Outline each blood parasite and name the species.
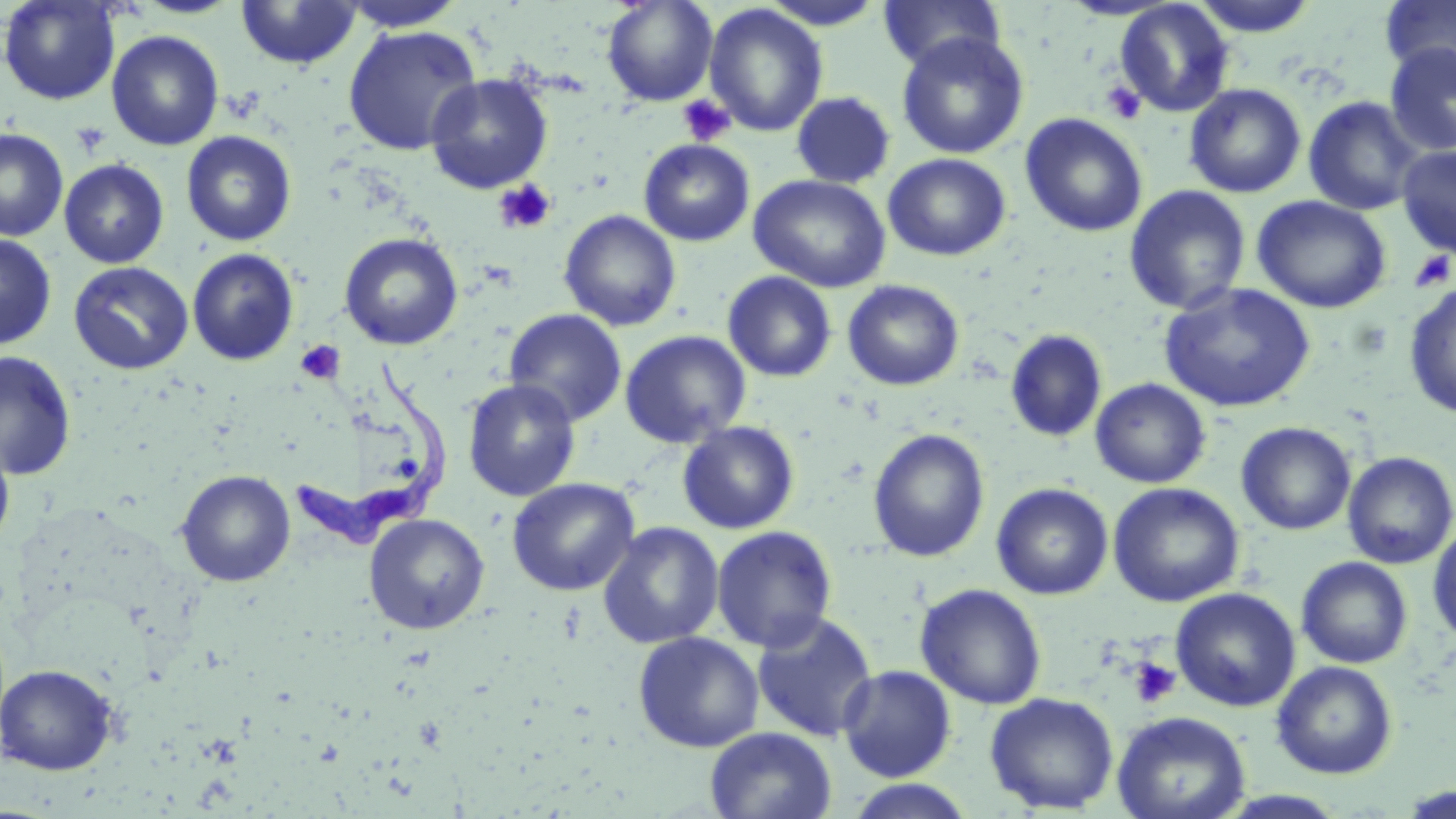

Approximate bounding boxes as (x1,y1)-(x2,y2) corner pairs in pixels.
Trypanosoma brucei: (289,361)-(452,548).
No Plasmodium falciparum, Plasmodium ovale, Plasmodium malariae, Plasmodium vivax, or Babesia divergens observed.

Summary:
  - Uninfected red blood cell locations: (0,0)-(121,105), (133,0)-(243,19), (339,0)-(464,32), (601,0)-(718,106), (758,0)-(886,29), (879,0)-(1005,72), (1059,0)-(1180,21), (1189,0)-(1320,37), (1379,0)-(1456,84), (235,1)-(362,70), (1114,1)-(1235,117), (703,4)-(829,137), (342,24)-(482,155), (106,30)-(224,151), (896,32)-(1029,160), (1384,42)-(1456,156), (425,73)-(553,194), (1184,83)-(1306,198), (791,92)-(895,188), (1303,96)-(1424,216), (1020,113)-(1148,238), (0,128)-(68,241), (181,130)-(297,246), (639,139)-(755,246), (1397,144)-(1456,258), (883,153)-(1011,261), (59,159)-(169,268), (748,174)-(892,293), (1124,185)-(1251,315), (1252,195)-(1392,313), (559,210)-(681,332), (339,232)-(463,350), (0,233)-(56,350), (187,248)-(299,366), (69,261)-(193,375), (723,271)-(837,382), (843,279)-(964,391), (1403,281)-(1456,419), (1159,283)-(1316,413), (504,308)-(627,427), (1005,328)-(1107,443), (619,330)-(752,449), (0,351)-(77,480), (1090,378)-(1211,489), (463,379)-(581,501), (677,421)-(800,534), (1236,421)-(1356,535), (867,428)-(990,563), (0,438)-(15,552), (1342,451)-(1456,569), (176,470)-(295,587), (507,478)-(639,596), (991,482)-(1113,600), (1108,482)-(1244,607), (364,514)-(489,634), (1428,521)-(1456,645), (598,522)-(724,649), (711,525)-(837,652), (1296,556)-(1413,669), (915,583)-(1047,709), (1170,587)-(1301,712), (751,610)-(878,743), (633,632)-(764,753), (1272,661)-(1398,779), (0,664)-(119,775), (837,664)-(956,782), (984,692)-(1119,814), (1112,711)-(1250,819), (705,727)-(836,819), (844,779)-(977,818), (1396,782)-(1455,816), (1217,790)-(1350,817)
  - Platelet locations: (1101,80)-(1147,124), (678,95)-(736,147), (71,121)-(111,157), (493,180)-(557,235), (1409,251)-(1454,292), (294,339)-(345,385), (1128,656)-(1182,709)
  - Slide-level diagnosis: Trypanosoma brucei
  - Modality: optical microscopy
  - Field of view: single
  - Image size: 1456×819 pixels
  - Stain: May-Grünwald-Giemsa
  - Preparation: thin blood smear
  - Magnification: 1000x